Describe the morphology of the red blood cells.
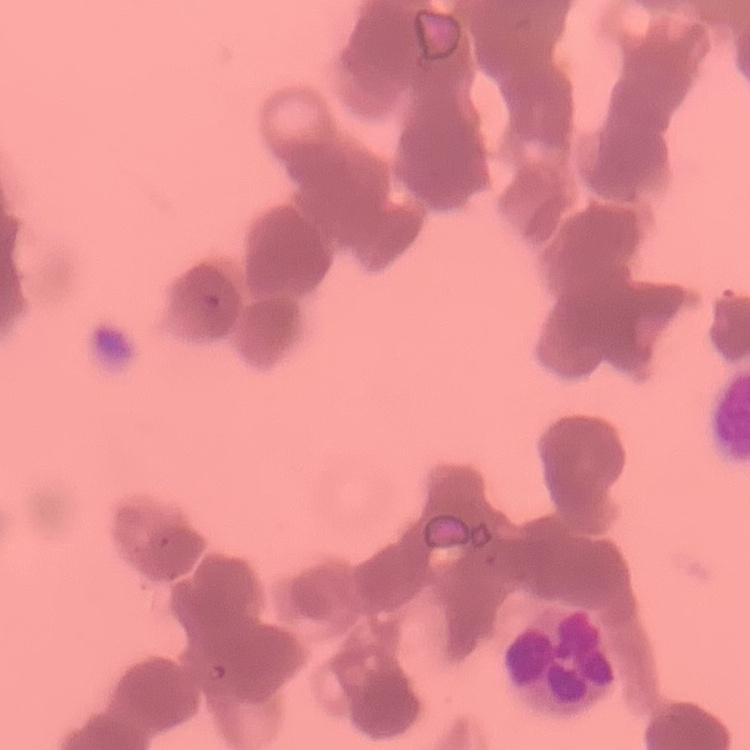
They show rouleaux formation.

Summary:
  - Image type: one tile cut from a larger photomicrograph
  - Preparation: thin blood smear
  - Stain: Field's or Giemsa